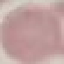

Result: no malaria parasites detected. Giemsa stain. Cell patch, automatically extracted from a larger field of view and resized to 64 × 64 pixels. Photographed with a smartphone camera at the microscope eyepiece. Thin blood smear.